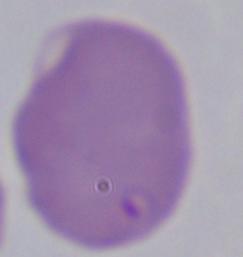
Summary:
  - Identification: Babesia
  - Modality: micrograph
  - Magnification: 1000x